Evaluate for malaria.
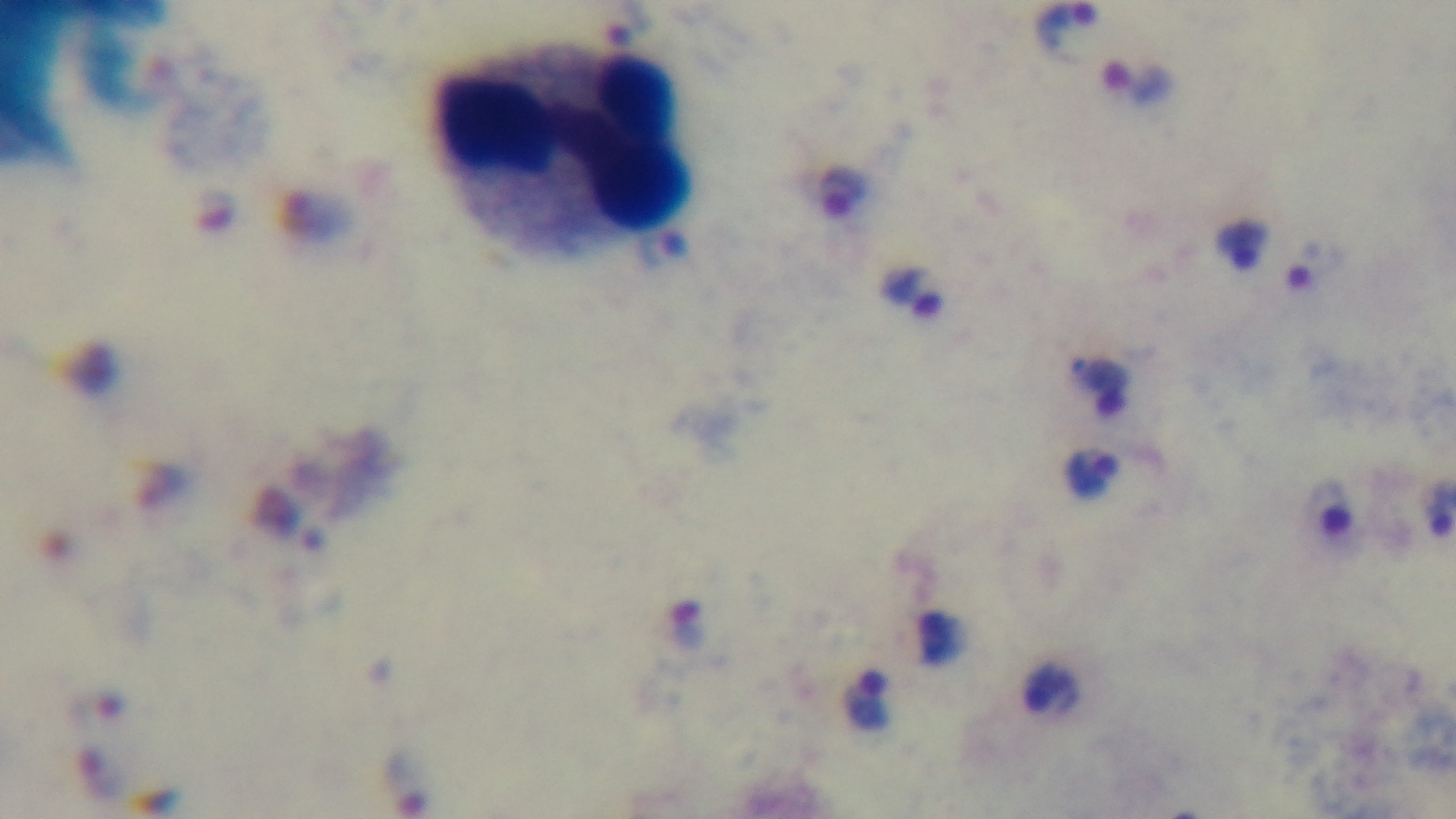

Positive.

Summary:
  - Stain: Giemsa
  - Preparation: thick smear
  - Objective: 100x oil immersion
  - Field of view: single
  - Modality: light microscopy
  - Capture: mounted 4K digital camera